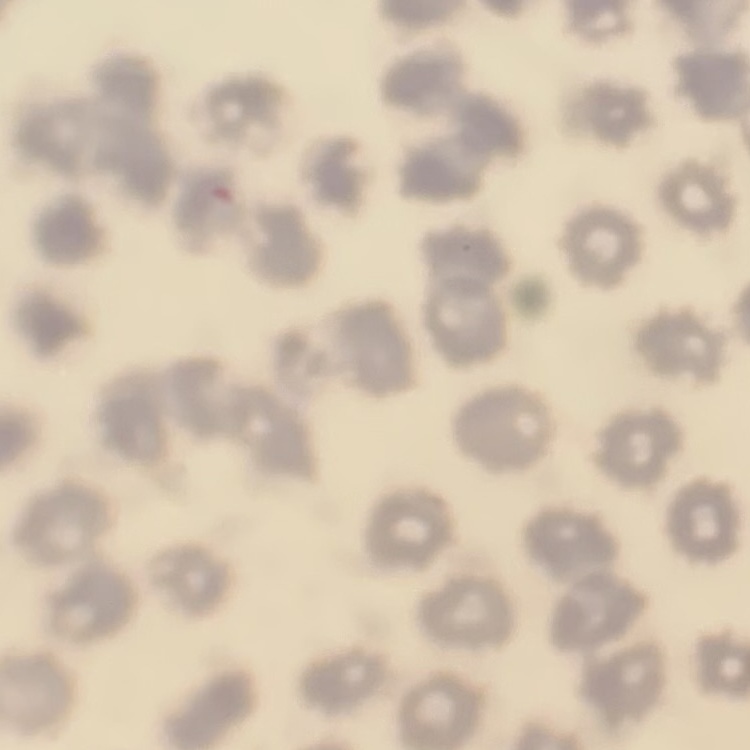 The red blood cells exhibit no rouleaux formation. Thin peripheral smear. Stained with either Field's or Giemsa. One tile cut from a larger photomicrograph.